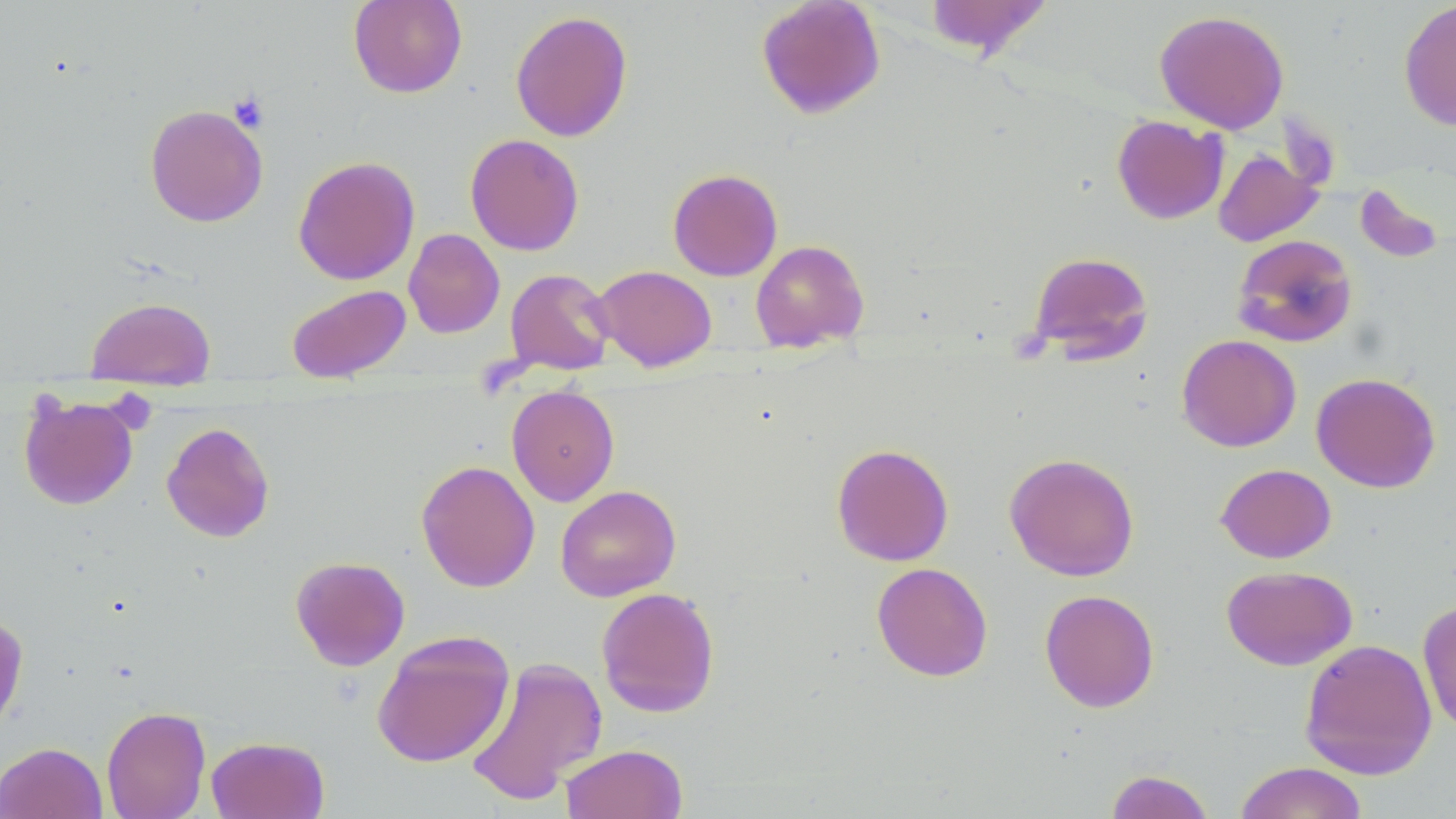
slide_level_diagnosis: negative for blood parasites
field_of_view: single
uninfected_red_blood_cell_locations: 'approximate bounding boxes as (x1,y1)-(x2,y2) corner pairs in pixels: (348,0)-(467,98), (755,0)-(886,119), (923,0)-(1053,61), (1398,0)-(1456,132), (510,9)-(633,143), (1154,9)-(1289,134), (144,104)-(269,227), (1112,115)-(1228,224), (464,133)-(584,255), (1213,148)-(1323,247), (293,155)-(420,286), (667,168)-(783,281), (1353,182)-(1447,266), (403,228)-(505,338), (1232,234)-(1358,348), (750,239)-(869,353), (1027,250)-(1154,364), (592,265)-(717,372), (505,268)-(615,376), (287,284)-(411,383), (85,296)-(216,382), (1177,334)-(1301,452), (1311,372)-(1441,493), (506,384)-(620,506), (18,392)-(139,510), (162,422)-(275,542), (831,443)-(954,566), (1004,452)-(1140,582), (416,460)-(540,592), (1216,463)-(1336,563), (555,484)-(681,602), (290,555)-(410,671), (872,562)-(993,681), (1221,565)-(1357,671), (596,587)-(721,717), (1039,589)-(1160,712), (1417,599)-(1456,736), (0,611)-(29,736), (371,631)-(515,769), (1299,638)-(1437,780), (465,655)-(608,806), (101,705)-(211,819), (206,735)-(329,819), (0,742)-(107,819), (559,744)-(688,819), (1233,761)-(1368,819), (1104,769)-(1216,819)'
modality: optical microscopy
stain: May-Grünwald-Giemsa
platelet_locations: 'approximate bounding boxes as (x1,y1)-(x2,y2) corner pairs in pixels: (228,91)-(270,132)'
preparation: thin blood film
magnification: 1000x
image_size: 1456×819 pixels